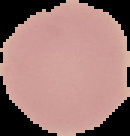
image size = 130×136 pixels
image type = segmented cell region with the area outside set to black
preparation = thin blood film
result = no malaria parasites seen